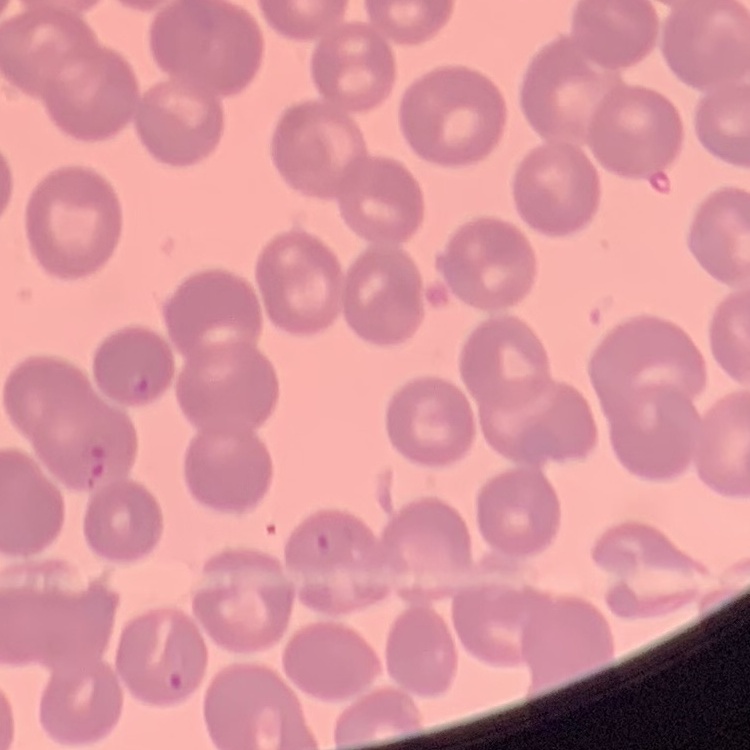 The erythrocytes show no rouleaux formation. Thin blood smear. One tile cut from a larger photomicrograph. Stained with either Field's or Giemsa.